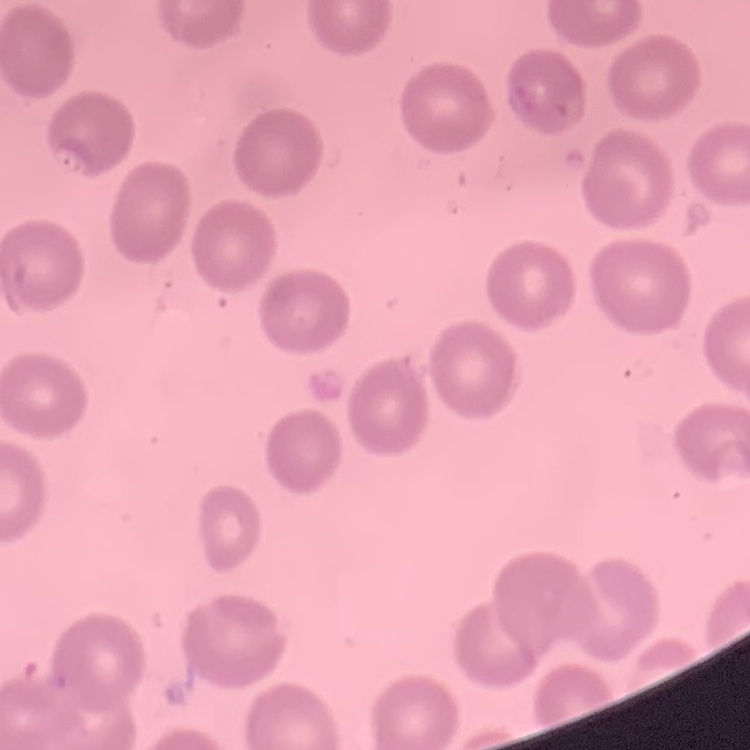
erythrocyte morphology = no rouleaux formation
image type = square crop of a larger photomicrograph
preparation = thin peripheral smear
stain = Field's or Giemsa